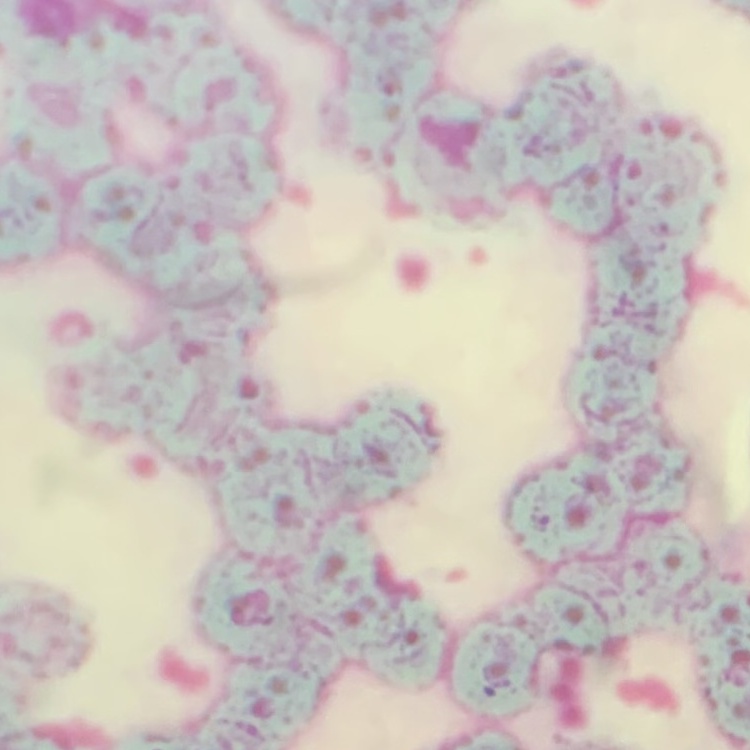

The red blood cells show rouleaux formation. Stained with either Field's or Giemsa. One tile cut from a larger photomicrograph. Thin blood smear.